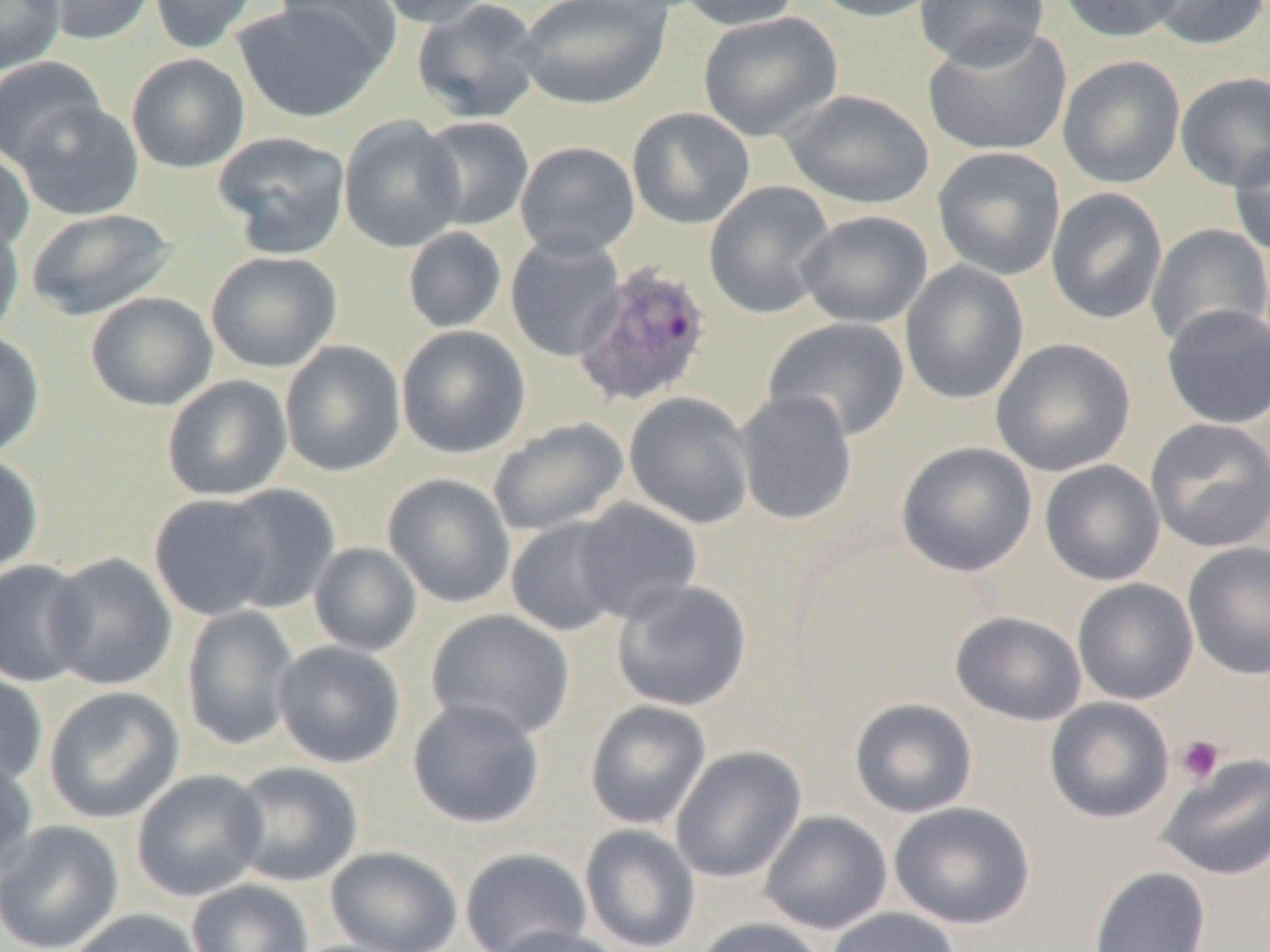
Approximate bounding boxes as (x1,y1)-(x2,y2) corner pairs in pixels. Platelet locations: (1175,735)-(1225,785). Plasmodium ovale-infected red blood cell locations: (573,261)-(714,407). Uninfected red blood cell locations: (0,0)-(66,73), (34,0)-(157,45), (149,0)-(259,54), (274,0)-(401,72), (369,0)-(500,27), (411,0)-(545,123), (515,0)-(673,110), (673,0)-(804,31), (807,0)-(946,23), (914,0)-(1051,69), (1057,0)-(1188,43), (1142,0)-(1270,51), (232,2)-(391,123), (698,11)-(843,141), (922,23)-(1073,157), (126,53)-(250,173), (1057,55)-(1186,189), (0,56)-(108,171), (1175,71)-(1270,191), (780,89)-(935,210), (13,100)-(144,220), (627,107)-(756,229), (416,115)-(536,231), (339,116)-(466,253), (212,131)-(351,258), (1228,140)-(1270,257), (515,141)-(640,259), (932,146)-(1066,281), (0,147)-(36,256), (703,181)-(837,319), (1045,187)-(1168,325), (25,208)-(177,321), (797,210)-(933,329), (0,215)-(25,343), (1146,224)-(1270,349), (402,226)-(508,333), (504,233)-(625,362), (205,251)-(343,373), (899,260)-(1030,405), (85,292)-(218,411), (1160,304)-(1270,429), (763,317)-(911,443), (396,325)-(531,459), (0,330)-(45,460), (991,338)-(1136,477), (279,340)-(406,477), (161,375)-(293,502), (734,391)-(859,525), (624,392)-(756,529), (487,417)-(630,538), (1145,418)-(1270,553), (896,442)-(1037,577), (0,450)-(44,579), (1040,460)-(1166,586), (382,473)-(516,608), (213,485)-(341,613), (148,493)-(280,621), (570,498)-(703,625), (506,515)-(630,637), (309,542)-(422,656), (1183,542)-(1270,680), (44,553)-(178,691), (0,559)-(93,687), (611,579)-(752,712), (1073,579)-(1199,704), (181,606)-(301,751), (425,609)-(576,741), (950,611)-(1087,726), (273,640)-(406,768), (0,671)-(48,792), (43,686)-(185,824), (1045,697)-(1175,824), (850,698)-(979,818), (407,699)-(546,829), (585,700)-(712,830), (671,745)-(806,883), (1156,753)-(1270,881), (0,755)-(40,882), (226,761)-(364,887), (131,769)-(268,902), (889,802)-(1035,929), (759,811)-(893,934), (0,820)-(124,952), (579,824)-(701,952), (325,846)-(463,952), (460,847)-(593,952), (1088,866)-(1211,952), (186,879)-(315,952), (826,907)-(961,952), (66,908)-(207,952), (695,917)-(828,952), (490,926)-(629,952). Slide-level diagnosis: Plasmodium ovale. Thin blood film. Light microscopy. Single field of view. Image is 1270×952 pixels. Captured at 1000x magnification.